Locate Plasmodium parasites and leukocytes.
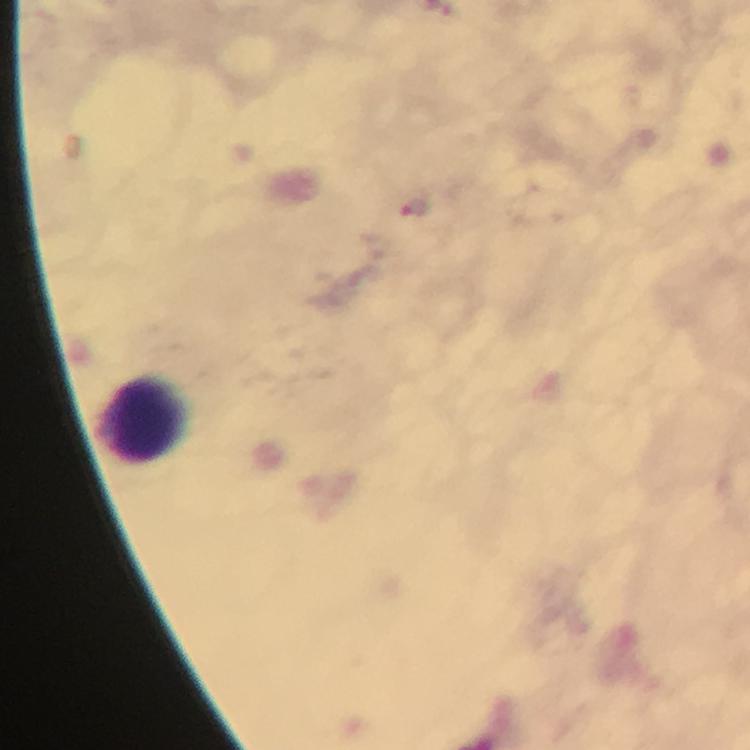

Approximate centers as [x, y] in pixels.
Plasmodium parasites: [411, 209].
Leukocytes: [143, 417].

{
  "immersion_oil": "applied",
  "capture": "smartphone camera through the microscope",
  "stain": "Giemsa",
  "cropped_from": "a single field of view",
  "magnification": "100x",
  "preparation": "thick blood smear",
  "image_size": "750×750 pixels",
  "context": "from a malaria diagnostic workup"
}